Report the malaria status of this cell.
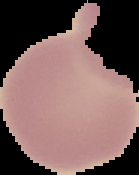

It is uninfected.

image_size: 139×175 pixels
image_type: segmented cell region with the area outside set to black
preparation: thin blood film